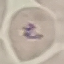

{
  "result": "no malaria parasites detected",
  "capture": "smartphone through the microscope eyepiece",
  "preparation": "thin blood film",
  "stain": "Giemsa",
  "image_type": "automatically extracted cell patch, resized to 64 × 64 pixels"
}